Name the cell type shown.
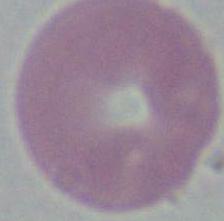

An erythrocyte.

{
  "modality": "photomicrograph",
  "magnification": "1000x"
}